Give the extent of all uninfected red blood cells.
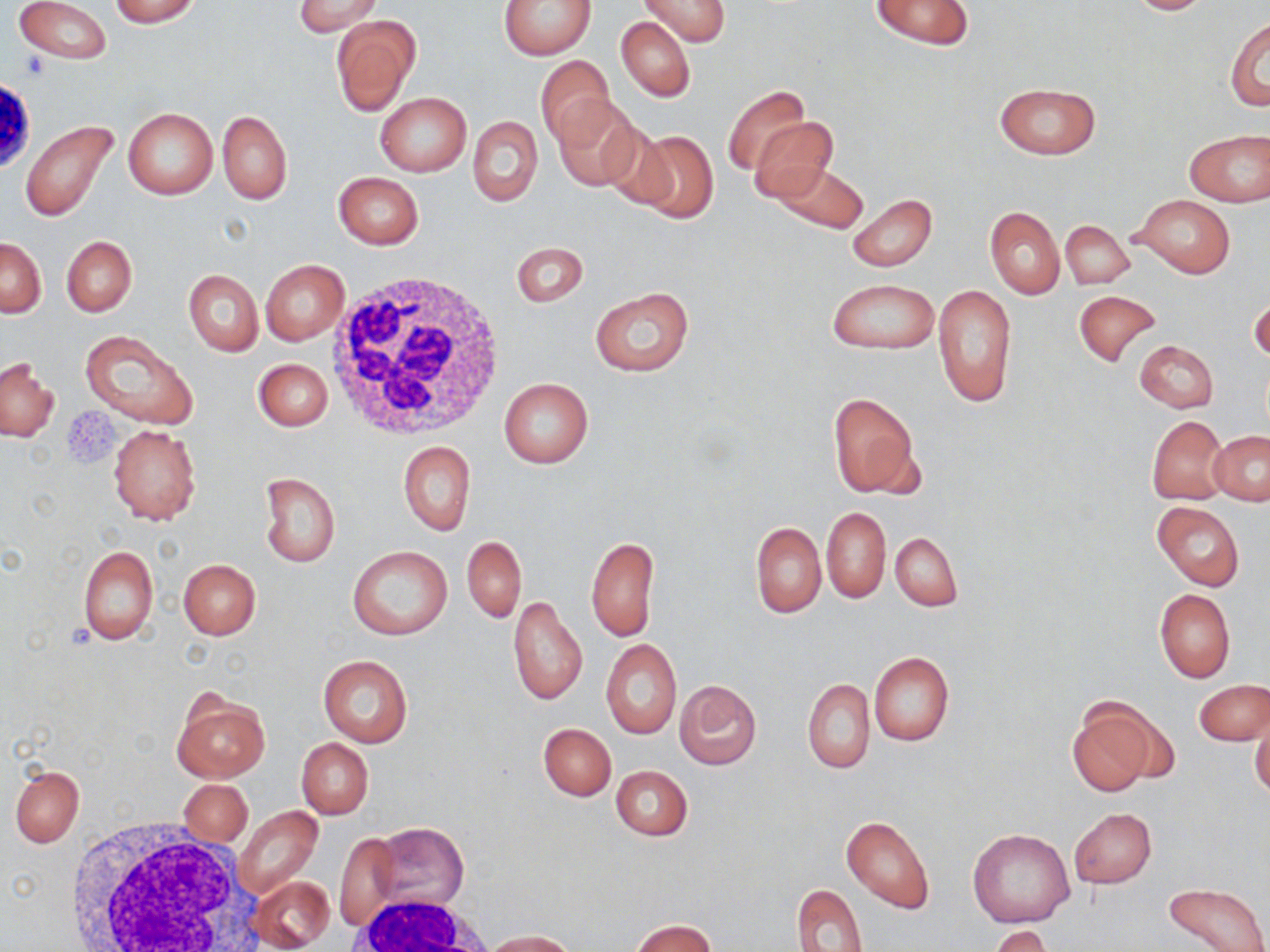
Approximate bounding boxes as [x1, y1, x2, y2] in pixels.
Uninfected red blood cells: [13, 0, 111, 63], [108, 0, 201, 26], [292, 0, 384, 36], [499, 0, 595, 58], [638, 0, 728, 46], [870, 0, 974, 49], [1119, 0, 1218, 15], [331, 16, 421, 115], [1225, 16, 1269, 111], [616, 17, 696, 102], [537, 55, 617, 146], [995, 83, 1099, 159], [724, 86, 809, 176], [375, 91, 471, 176], [552, 101, 643, 192], [122, 107, 217, 199], [218, 110, 291, 204], [469, 116, 542, 206], [749, 117, 837, 203], [20, 119, 118, 222], [1184, 129, 1270, 207], [630, 130, 718, 225], [774, 162, 868, 233], [333, 172, 423, 249], [848, 193, 937, 271], [1133, 195, 1234, 277], [985, 207, 1064, 299], [1061, 220, 1134, 288], [61, 235, 136, 316], [0, 237, 46, 318], [511, 240, 587, 308], [261, 259, 349, 345], [183, 270, 263, 356], [828, 279, 936, 355], [933, 283, 1017, 407], [589, 287, 695, 375], [1074, 289, 1160, 366], [1249, 293, 1269, 365], [79, 330, 198, 429], [1134, 340, 1218, 412], [1, 357, 57, 442], [253, 358, 333, 432], [498, 377, 593, 468], [826, 390, 922, 499], [1146, 416, 1228, 504], [108, 424, 201, 526], [1208, 431, 1269, 506], [399, 439, 475, 535], [258, 472, 341, 567], [1153, 501, 1244, 590], [821, 507, 890, 603], [750, 522, 826, 618], [891, 532, 962, 611], [462, 536, 525, 623], [585, 536, 659, 642], [78, 543, 159, 647], [346, 546, 453, 640], [178, 559, 260, 638], [1155, 588, 1235, 682], [507, 597, 588, 706], [601, 639, 682, 737], [869, 652, 954, 747], [318, 655, 413, 746], [802, 678, 874, 773], [1195, 679, 1269, 744], [674, 680, 762, 770], [171, 691, 270, 782], [1068, 701, 1160, 796], [1251, 714, 1269, 801], [539, 723, 615, 800], [296, 738, 374, 819], [10, 764, 86, 846], [610, 765, 693, 840], [179, 779, 252, 847], [231, 806, 323, 901], [1068, 808, 1156, 888], [841, 815, 934, 913], [373, 821, 470, 916], [968, 829, 1074, 928], [334, 832, 401, 929], [252, 876, 334, 951], [1162, 881, 1268, 952], [793, 884, 867, 951], [629, 919, 718, 952], [988, 926, 1054, 952], [484, 930, 576, 951].

{
  "slide_level_diagnosis": "no evidence of blood parasites",
  "white_blood_cell_locations": "approximate bounding boxes as [x1, y1, x2, y2] in pixels: [327, 268, 507, 441], [63, 816, 254, 952], [351, 894, 495, 952]",
  "field_of_view": "single",
  "magnification": "1000x",
  "modality": "optical microscopy",
  "image_size": "1270×952 pixels",
  "preparation": "thin blood film",
  "stain": "May-Grünwald-Giemsa",
  "platelet_locations": "approximate bounding boxes as [x1, y1, x2, y2] in pixels: [18, 52, 51, 80]"
}